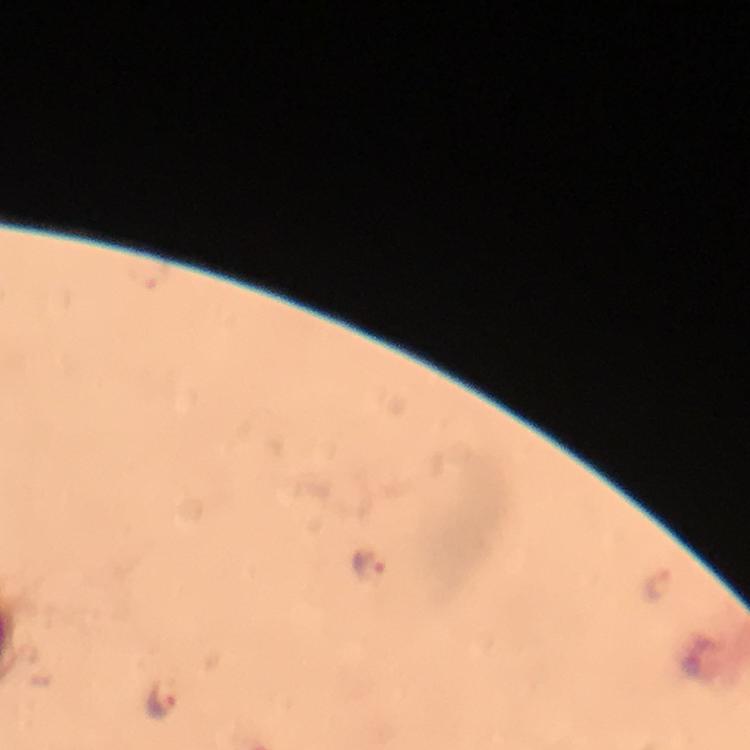 Approximate centers as (x, y) in pixels. Malaria parasite locations: (368, 565), (659, 582), (163, 701). Image is 750×750 pixels. Cropped region of a single field of view. Photographed through the microscope with a smartphone camera. Thick blood film. Giemsa-stained preparation. At 100x magnification. Immersion oil applied. From a diagnostic examination for malaria.